State which cell type is depicted.
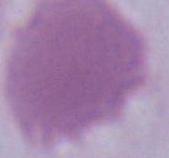

An erythrocyte.

1000x magnification. Photomicrograph.